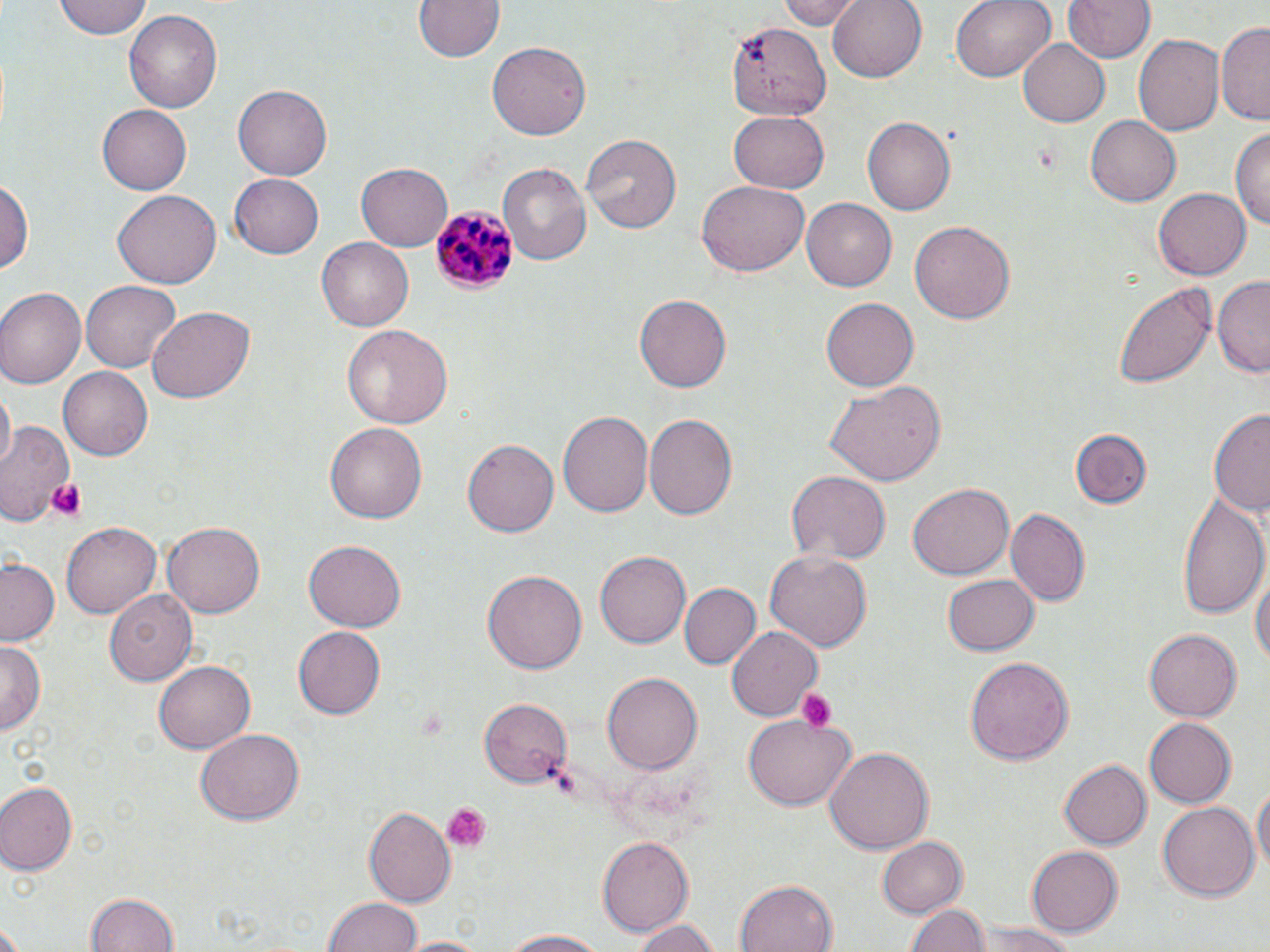
Summary:
  - Coordinate format: approximate bounding boxes as (x1, y1, x2, y2) in pixels
  - Uninfected red blood cell locations: (55, 0, 152, 39), (412, 0, 506, 63), (776, 0, 864, 28), (828, 0, 927, 83), (951, 0, 1056, 83), (1060, 0, 1157, 64), (123, 10, 223, 113), (726, 20, 829, 120), (1218, 20, 1270, 126), (1133, 34, 1225, 138), (1018, 37, 1111, 127), (486, 41, 590, 141), (234, 84, 333, 179), (99, 103, 195, 195), (727, 110, 828, 194), (1086, 115, 1181, 206), (863, 118, 955, 214), (1232, 125, 1270, 233), (580, 134, 684, 234), (357, 159, 453, 250), (498, 162, 593, 265), (230, 172, 325, 258), (1, 178, 34, 279), (697, 182, 809, 278), (112, 188, 219, 285), (1152, 188, 1250, 280), (802, 198, 897, 290), (909, 218, 1012, 323), (316, 237, 415, 331), (1212, 275, 1269, 378), (81, 280, 180, 374), (1115, 283, 1217, 389), (0, 289, 84, 391), (636, 294, 732, 393), (820, 298, 916, 391), (146, 306, 254, 403), (343, 326, 454, 429), (60, 367, 153, 461), (827, 380, 944, 487), (2, 387, 15, 468), (1208, 408, 1270, 519), (558, 411, 654, 517), (643, 416, 737, 524), (0, 417, 77, 525), (325, 423, 426, 525), (1070, 428, 1152, 509), (464, 439, 559, 538), (784, 471, 890, 566), (908, 482, 1014, 580), (1178, 491, 1268, 616), (1006, 508, 1090, 606), (163, 519, 264, 614), (61, 522, 161, 616), (303, 541, 405, 632), (764, 547, 870, 651), (595, 552, 689, 649), (0, 559, 60, 646), (1251, 559, 1269, 676), (483, 569, 586, 672), (942, 573, 1039, 656), (679, 583, 760, 670), (104, 588, 198, 687), (726, 626, 824, 720), (294, 627, 385, 719), (1146, 627, 1243, 721), (0, 640, 45, 736), (963, 656, 1072, 768), (154, 659, 256, 753), (604, 673, 700, 775), (480, 697, 572, 785), (743, 715, 856, 812), (1145, 718, 1237, 808), (196, 730, 304, 823), (826, 747, 932, 854), (1057, 758, 1150, 851), (1252, 781, 1269, 884), (0, 782, 78, 875), (1157, 801, 1258, 901), (364, 807, 455, 907), (878, 835, 968, 918), (597, 837, 691, 937), (1026, 843, 1121, 937), (734, 880, 835, 952), (85, 892, 182, 952), (324, 895, 422, 952), (907, 903, 986, 952), (631, 917, 723, 950), (975, 924, 1079, 952), (499, 928, 612, 950), (393, 936, 491, 952)
  - Platelet locations: (1035, 141, 1061, 175), (43, 476, 88, 522), (796, 688, 836, 734), (441, 803, 488, 852)
  - Plasmodium malariae-infected red blood cell locations: (430, 203, 519, 295)
  - Slide-level diagnosis: Plasmodium malariae
  - Field of view: one of a larger specimen
  - Modality: optical microscopy
  - Stain: May-Grünwald-Giemsa
  - Image size: 1270×952 pixels
  - Magnification: 1000x
  - Preparation: thin blood smear